Name the blood parasite species.
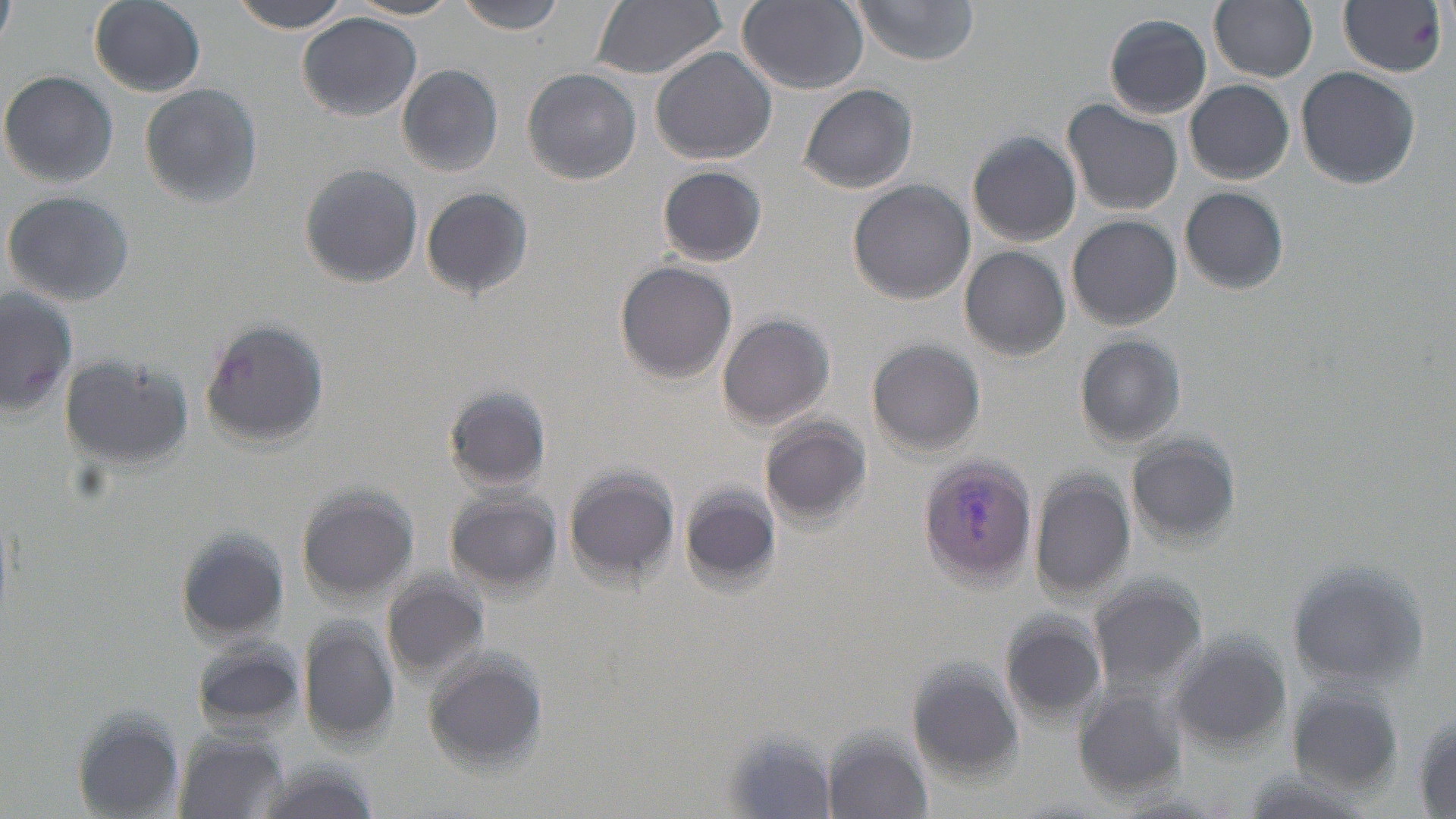

Plasmodium vivax.

stain = May-Grünwald-Giemsa
image size = 1456×819 pixels
field of view = single
uninfected red blood cell locations = approximate bounding boxes as (x1,y1)-(x2,y2) corner pairs in pixels: (0,0)-(16,47), (89,0)-(206,96), (230,0)-(355,33), (455,0)-(566,35), (589,0)-(728,79), (851,0)-(983,64), (1210,0)-(1317,81), (739,1)-(869,94), (298,13)-(423,121), (1103,14)-(1210,118), (650,46)-(776,166), (397,65)-(503,178), (1295,66)-(1420,190), (522,67)-(642,185), (1,71)-(118,188), (1185,79)-(1295,184), (139,82)-(263,210), (799,83)-(918,194), (1063,100)-(1182,216), (967,130)-(1082,249), (299,164)-(423,288), (658,166)-(765,266), (848,180)-(974,303), (420,186)-(533,298), (1180,187)-(1289,293), (3,190)-(135,308), (1066,215)-(1182,329), (959,247)-(1069,360), (614,260)-(738,384), (2,284)-(77,420), (715,313)-(835,429), (200,319)-(331,450), (1075,334)-(1186,449), (867,339)-(985,458), (59,353)-(191,468), (446,386)-(550,490), (758,414)-(871,526), (1126,434)-(1240,546), (564,469)-(678,584), (1028,471)-(1134,603), (297,485)-(418,604), (683,486)-(781,589), (445,490)-(557,594), (177,525)-(295,645), (1287,558)-(1427,691), (383,569)-(490,682), (1088,574)-(1207,697), (1002,611)-(1108,724), (298,619)-(402,750), (1167,629)-(1293,754), (190,638)-(303,734), (421,654)-(551,770), (907,660)-(1025,782), (1288,685)-(1407,797), (1073,692)-(1190,802), (1410,709)-(1456,814), (70,711)-(186,819), (821,730)-(935,819), (173,733)-(289,819)
preparation = thin blood film
magnification = 1000x
Plasmodium vivax-infected red blood cell locations = approximate bounding boxes as (x1,y1)-(x2,y2) corner pairs in pixels: (1339,0)-(1448,77), (916,458)-(1039,588)
modality = light microscopy